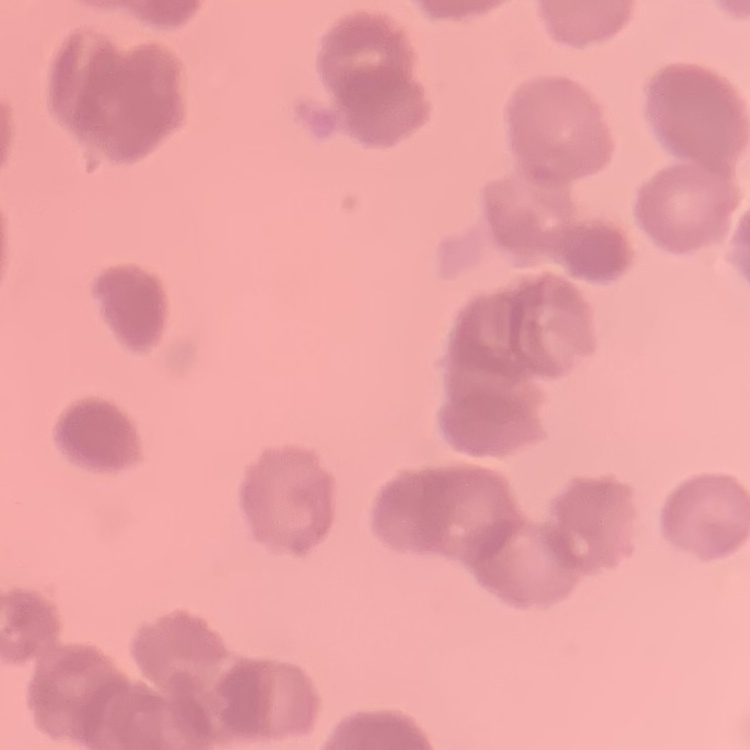
{
  "red_blood_cell_morphology": "rouleaux formation",
  "preparation": "thin peripheral smear",
  "image_type": "one tile cut from a larger photomicrograph",
  "stain": "Field's or Giemsa"
}